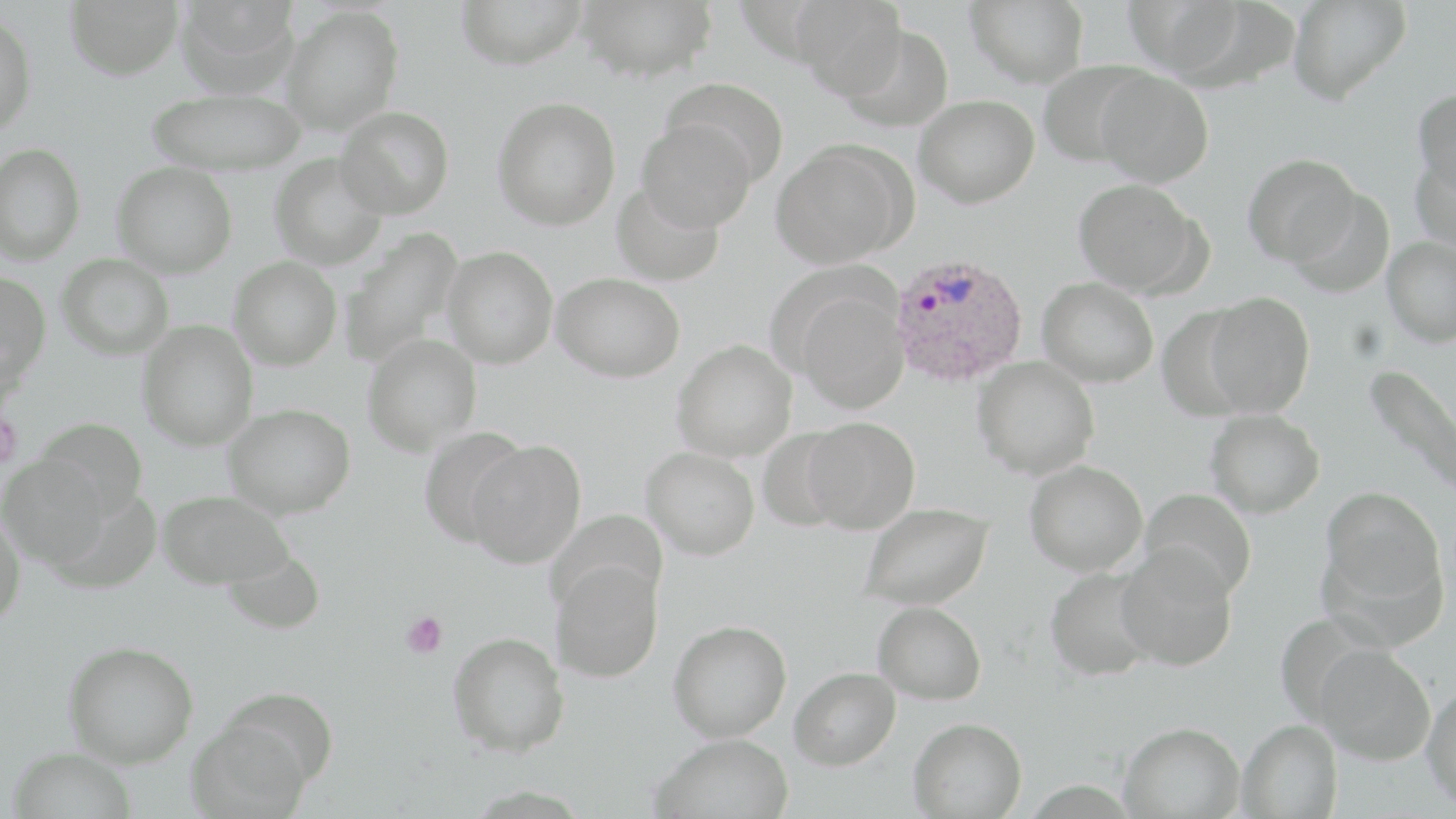
Approximate bounding boxes as (x1, y1, x2, y2) in pixels. Uninfected red blood cell locations: (64, 0, 184, 79), (175, 0, 302, 96), (456, 0, 587, 69), (578, 0, 718, 82), (791, 0, 909, 99), (965, 0, 1089, 88), (1124, 0, 1246, 80), (1288, 0, 1412, 104), (280, 4, 404, 136), (0, 12, 38, 136), (837, 23, 954, 132), (1037, 59, 1151, 168), (1093, 67, 1214, 187), (661, 77, 791, 187), (145, 87, 307, 174), (1413, 87, 1456, 197), (913, 93, 1040, 208), (492, 96, 621, 230), (336, 105, 454, 218), (636, 118, 755, 233), (771, 140, 911, 268), (1, 142, 86, 265), (1410, 150, 1456, 253), (270, 153, 389, 271), (1242, 154, 1362, 266), (112, 162, 237, 278), (1073, 178, 1203, 296), (611, 180, 725, 286), (1287, 189, 1395, 297), (337, 227, 465, 368), (1382, 236, 1456, 347), (442, 246, 558, 368), (57, 253, 174, 360), (229, 256, 343, 370), (0, 272, 51, 386), (552, 272, 685, 382), (1038, 277, 1159, 387), (794, 289, 909, 413), (1203, 291, 1315, 417), (1156, 306, 1255, 421), (137, 320, 258, 451), (362, 334, 482, 456), (672, 339, 797, 462), (972, 356, 1099, 480), (1362, 363, 1456, 502), (223, 403, 355, 518), (1205, 409, 1326, 518), (35, 416, 149, 521), (801, 416, 920, 533), (417, 427, 532, 549), (466, 440, 586, 568), (642, 446, 759, 559), (1, 453, 110, 568), (1024, 460, 1147, 576), (1320, 487, 1446, 615), (1139, 488, 1257, 602), (157, 489, 293, 588), (858, 502, 994, 610), (0, 508, 25, 631), (547, 509, 667, 614), (1116, 545, 1239, 672), (222, 548, 326, 635), (548, 558, 666, 683), (1044, 565, 1158, 681), (873, 601, 986, 704), (668, 619, 792, 741), (448, 630, 570, 755), (63, 640, 198, 767), (1314, 645, 1437, 764), (789, 666, 901, 770), (1421, 683, 1456, 811), (187, 712, 315, 818), (908, 716, 1027, 818), (1238, 719, 1342, 818), (1119, 721, 1245, 818), (652, 733, 793, 819), (7, 746, 136, 819). Plasmodium ovale-infected red blood cell locations: (889, 252, 1029, 387). Platelet locations: (402, 612, 448, 658). Slide-level diagnosis: Plasmodium ovale. Optical microscopy. Single field of view. 1000x magnification. Image is 1456×819 pixels. May-Grünwald-Giemsa-stained preparation. Thin blood film.